Identify the blood parasite species.
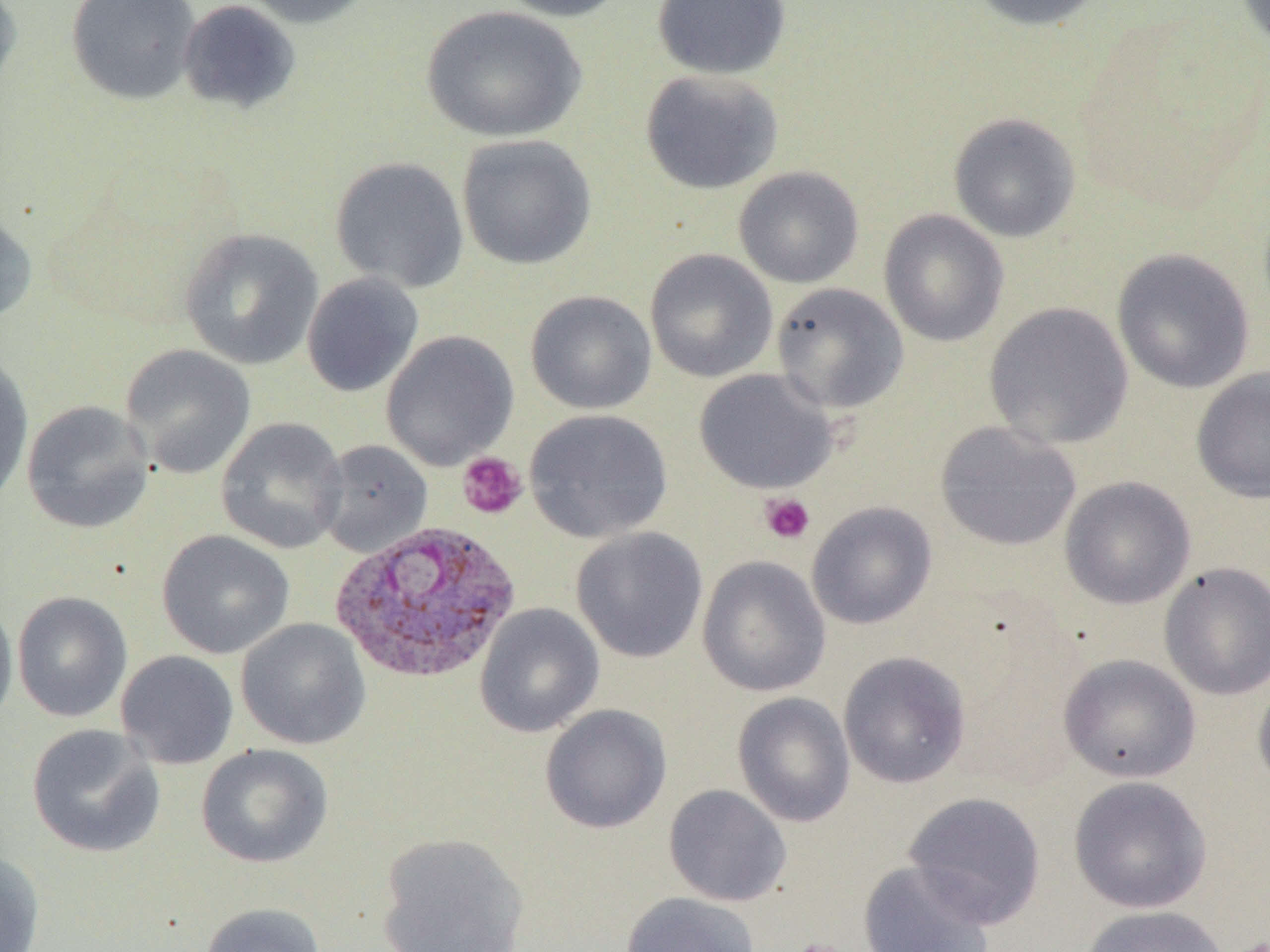

Plasmodium vivax.

Summary:
  - Coordinate format: approximate bounding boxes as (x1,y1)-(x2,y2) corner pairs in pixels
  - Plasmodium vivax-infected red blood cell locations: (330,519)-(521,684)
  - Platelet locations: (456,451)-(527,520), (759,493)-(815,544), (786,938)-(853,952)
  - Uninfected red blood cell locations: (65,0)-(201,105), (178,0)-(302,114), (237,0)-(376,29), (493,0)-(631,22), (652,0)-(791,80), (967,0)-(1109,32), (1235,0)-(1270,56), (0,2)-(23,97), (422,5)-(587,143), (640,70)-(784,194), (948,112)-(1081,243), (455,134)-(597,270), (329,156)-(469,294), (733,166)-(865,288), (0,207)-(38,326), (878,209)-(1009,347), (178,228)-(324,370), (644,248)-(778,383), (1111,248)-(1255,394), (301,272)-(424,397), (771,282)-(909,414), (525,290)-(657,414), (983,301)-(1134,450), (381,330)-(518,470), (119,344)-(257,480), (0,353)-(34,506), (1191,366)-(1270,503), (694,368)-(839,495), (22,400)-(155,534), (525,409)-(673,543), (216,417)-(348,554), (934,420)-(1082,552), (317,440)-(433,557), (1059,476)-(1196,609), (806,501)-(937,630), (571,527)-(708,663), (157,530)-(294,659), (697,555)-(831,697), (1159,562)-(1270,701), (12,591)-(132,722), (0,595)-(18,729), (475,603)-(605,737), (236,618)-(371,750), (116,650)-(238,769), (838,651)-(971,789), (1059,654)-(1202,783), (1253,674)-(1270,797), (732,692)-(856,827), (540,704)-(672,834), (26,723)-(165,858), (196,744)-(333,868), (1068,775)-(1211,914), (663,783)-(792,907), (904,791)-(1046,928), (376,832)-(530,952), (0,849)-(46,952), (858,860)-(997,952), (619,891)-(761,952), (200,902)-(326,952), (1079,904)-(1231,952)
  - Magnification: 1000x
  - Modality: optical microscopy
  - Preparation: thin blood film
  - Field of view: single
  - Image size: 1270×952 pixels